Describe the morphology of the erythrocytes.
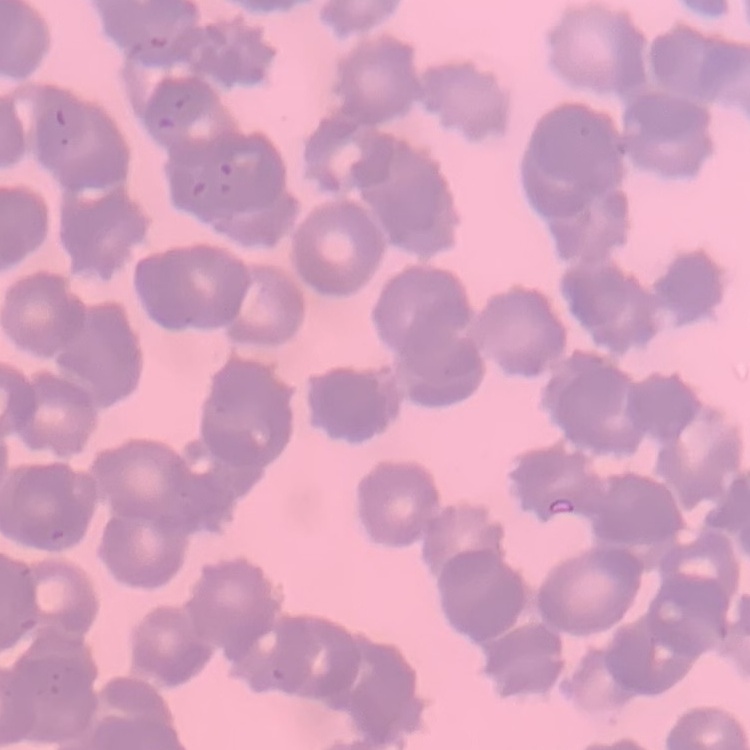
They show rouleaux formation.

preparation = thin blood film
stain = Field's or Giemsa
image type = square crop of a larger photomicrograph